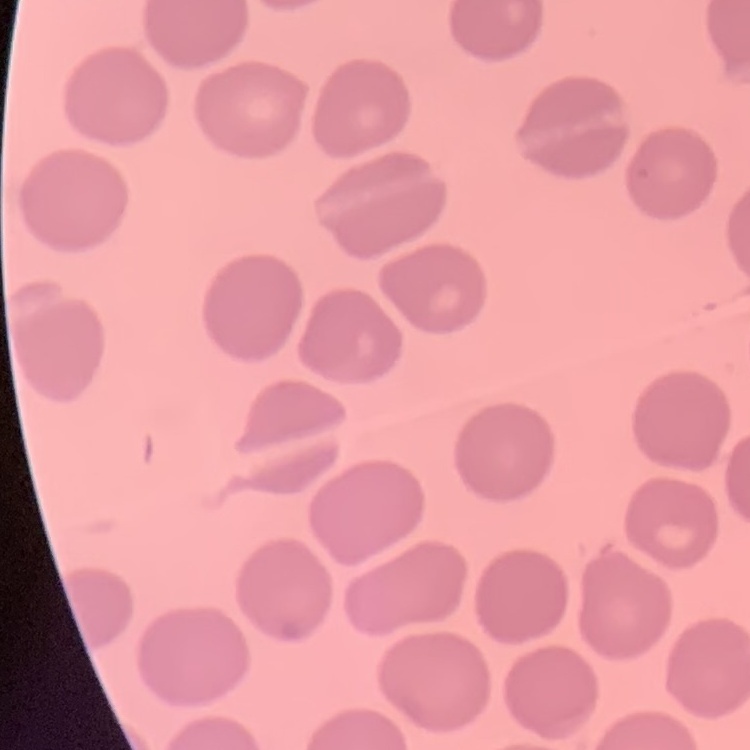 The red blood cells show no rouleaux formation. Thin peripheral smear. Square crop of a larger photomicrograph. Stained with either Field's or Giemsa.